Report the malaria status of this cell.
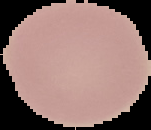
Uninfected.

From a thin blood film. Image is 151×130 pixels. Segmented cell region on a black background.